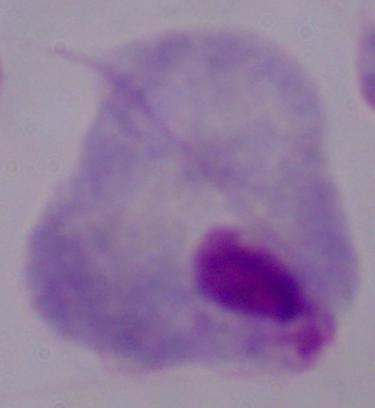

Photomicrograph. A trichomonad is shown. Captured at 1000x magnification.